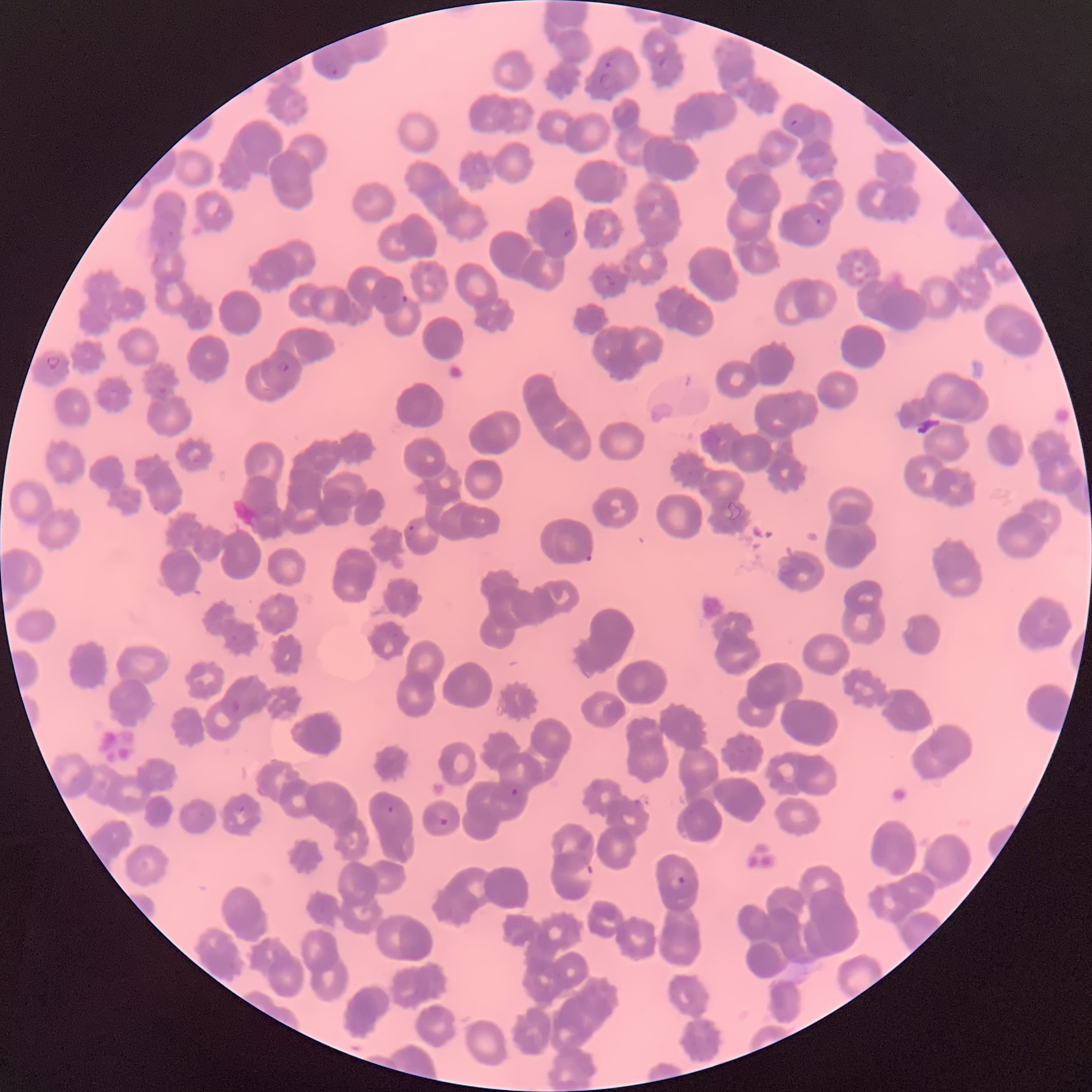
Approximate bounding boxes as (x1,y1)-(x2,y2) corner pairs in pixels. Plasmodium parasite locations: (658,56)-(667,69), (605,57)-(615,68), (324,63)-(340,77), (598,72)-(610,89), (791,118)-(798,127), (814,210)-(830,225), (563,228)-(574,239), (401,294)-(409,303), (45,356)-(61,371), (277,360)-(290,372), (158,386)-(167,394), (406,524)-(415,537), (584,553)-(592,562), (230,700)-(241,712), (510,787)-(519,796), (386,805)-(394,815), (439,818)-(449,827), (572,863)-(595,883), (676,874)-(688,886). Thin blood film. Optical microscopy. Image is 1092×1092 pixels. The red blood cells show rouleaux formation.